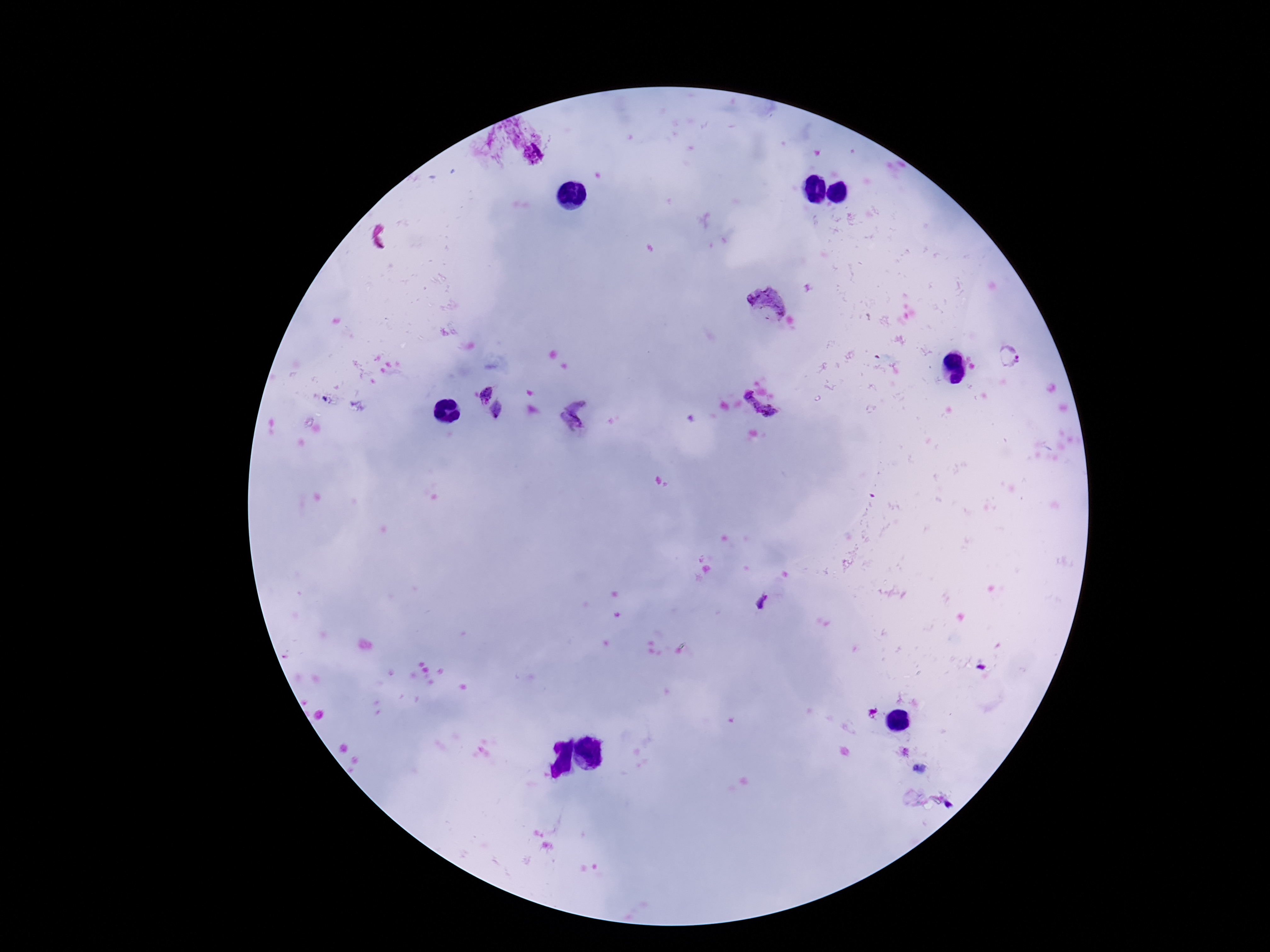
field of view = one from this slide
stain = Giemsa
magnification = 100x
patient malaria status = positive
preparation = thick peripheral-blood smear
capture = smartphone camera through the microscope eyepiece
image size = 1270×952 pixels
Plasmodium parasite locations = approximate object centers, in pixels from the top-left corner: (x=771, y=303), (x=1010, y=357), (x=484, y=392), (x=761, y=403), (x=496, y=411), (x=577, y=413), (x=760, y=602)